Give the position of every Plasmodium parasite.
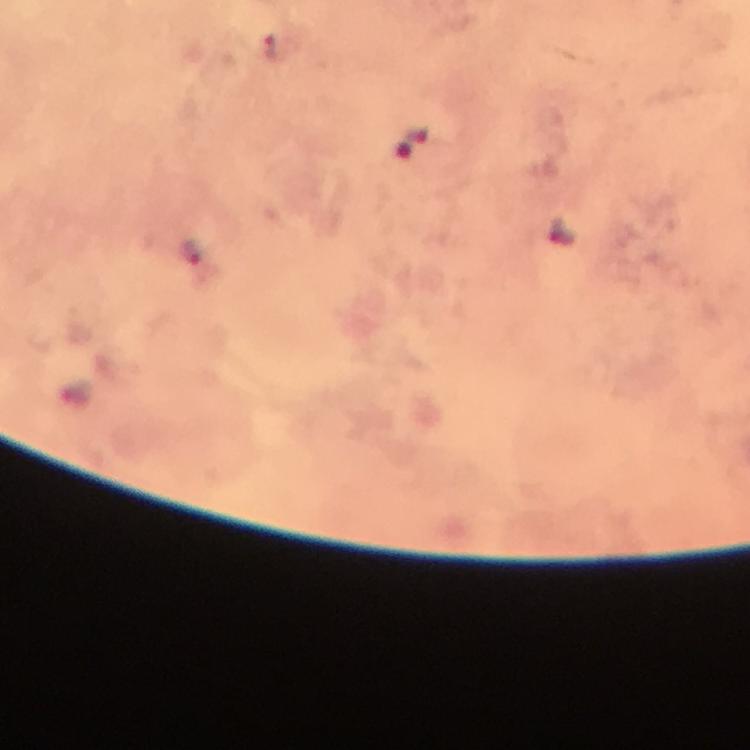
Approximate centers as (x, y) in pixels.
Plasmodium parasites: (270, 46).

Summary:
  - Image size: 750×750 pixels
  - Stain: Giemsa
  - Cropped from: one field of view
  - Context: from a malaria diagnostic workup
  - Immersion oil: applied
  - Magnification: 100x
  - Capture: smartphone photograph through a microscope
  - Preparation: thick smear